Locate every uninfected red blood cell.
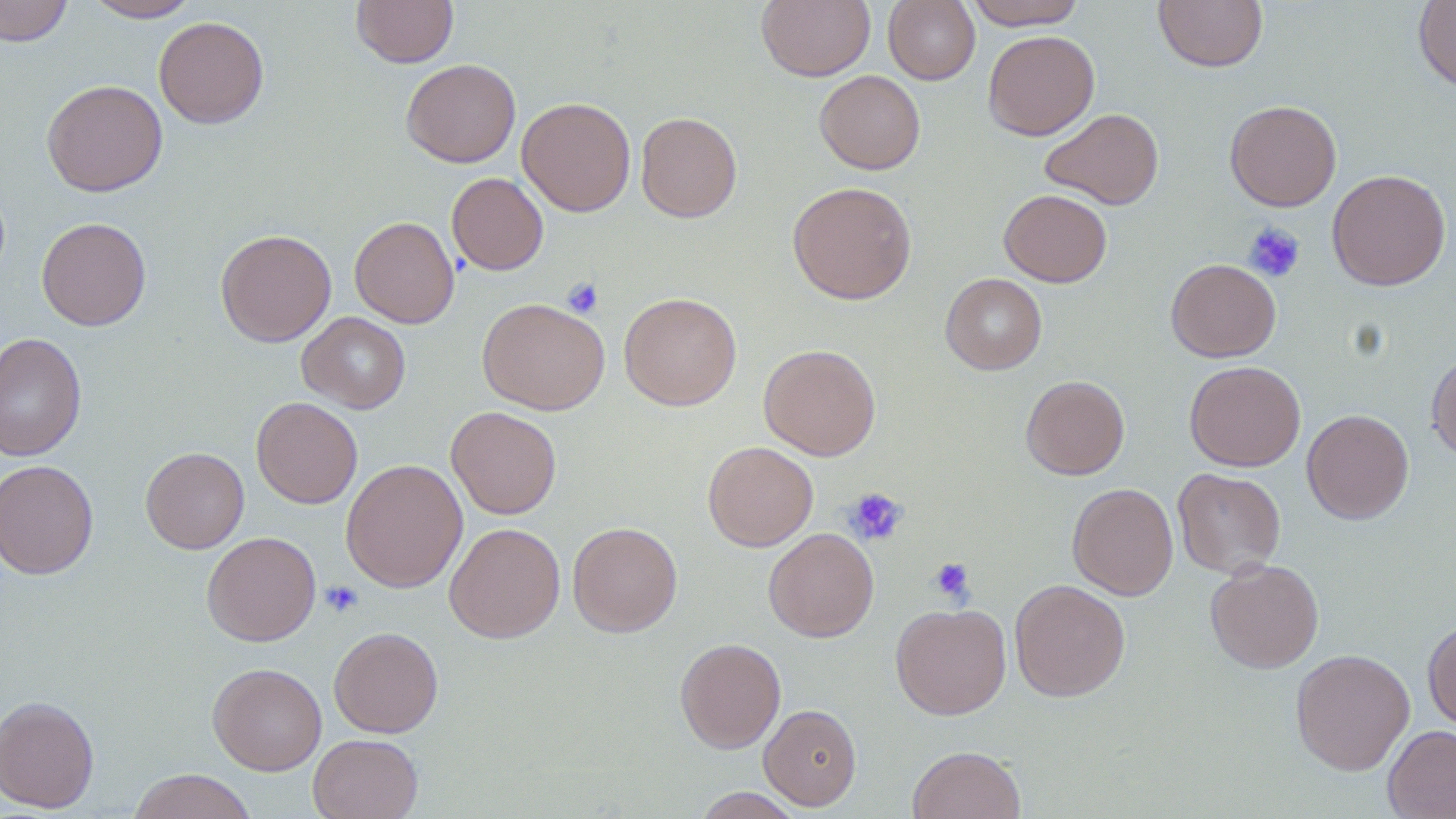

Approximate bounding boxes as [x1, y1, x2, y2] in pixels.
Uninfected red blood cells: [0, 0, 73, 46], [83, 0, 201, 22], [351, 0, 459, 67], [883, 0, 980, 85], [962, 0, 1089, 29], [1154, 0, 1268, 72], [757, 1, 875, 82], [1412, 1, 1456, 92], [153, 16, 269, 129], [983, 30, 1099, 141], [401, 58, 521, 168], [815, 70, 925, 175], [41, 79, 167, 197], [517, 96, 636, 216], [1224, 99, 1341, 211], [1040, 108, 1165, 209], [636, 112, 742, 222], [1327, 169, 1451, 290], [446, 172, 549, 275], [787, 181, 917, 305], [999, 189, 1112, 287], [36, 216, 152, 331], [350, 216, 460, 329], [215, 229, 336, 347], [1166, 258, 1281, 362], [940, 273, 1047, 375], [619, 292, 742, 411], [478, 298, 610, 415], [297, 312, 411, 414], [0, 331, 87, 462], [759, 343, 881, 460], [1426, 350, 1456, 462], [1184, 360, 1305, 471], [1020, 375, 1130, 480], [251, 396, 363, 508], [446, 407, 562, 519], [1301, 408, 1414, 524], [703, 441, 818, 551], [141, 447, 249, 554], [341, 459, 468, 592], [0, 460, 99, 580], [1172, 468, 1286, 579], [1067, 482, 1178, 600], [568, 521, 683, 637], [444, 522, 566, 643], [763, 527, 878, 642], [202, 531, 321, 646], [1205, 559, 1323, 674], [1009, 578, 1131, 702], [890, 602, 1011, 720], [1422, 618, 1456, 733], [329, 626, 444, 737], [674, 637, 786, 753], [1290, 648, 1415, 775], [207, 662, 327, 775], [0, 695, 100, 813], [759, 704, 862, 810], [1383, 725, 1456, 819], [308, 733, 424, 819], [907, 745, 1027, 819], [127, 768, 258, 819], [692, 787, 803, 818].

Platelet locations: [1243, 222, 1306, 283], [562, 276, 603, 318], [843, 487, 908, 546], [928, 558, 975, 603], [321, 580, 364, 618]. Slide-level diagnosis: negative for blood parasites. Single field of view. May-Grünwald-Giemsa stain. Image is 1456×819 pixels. Optical microscopy. Thin blood smear. 1000x magnification.